Identify the blood parasite species.
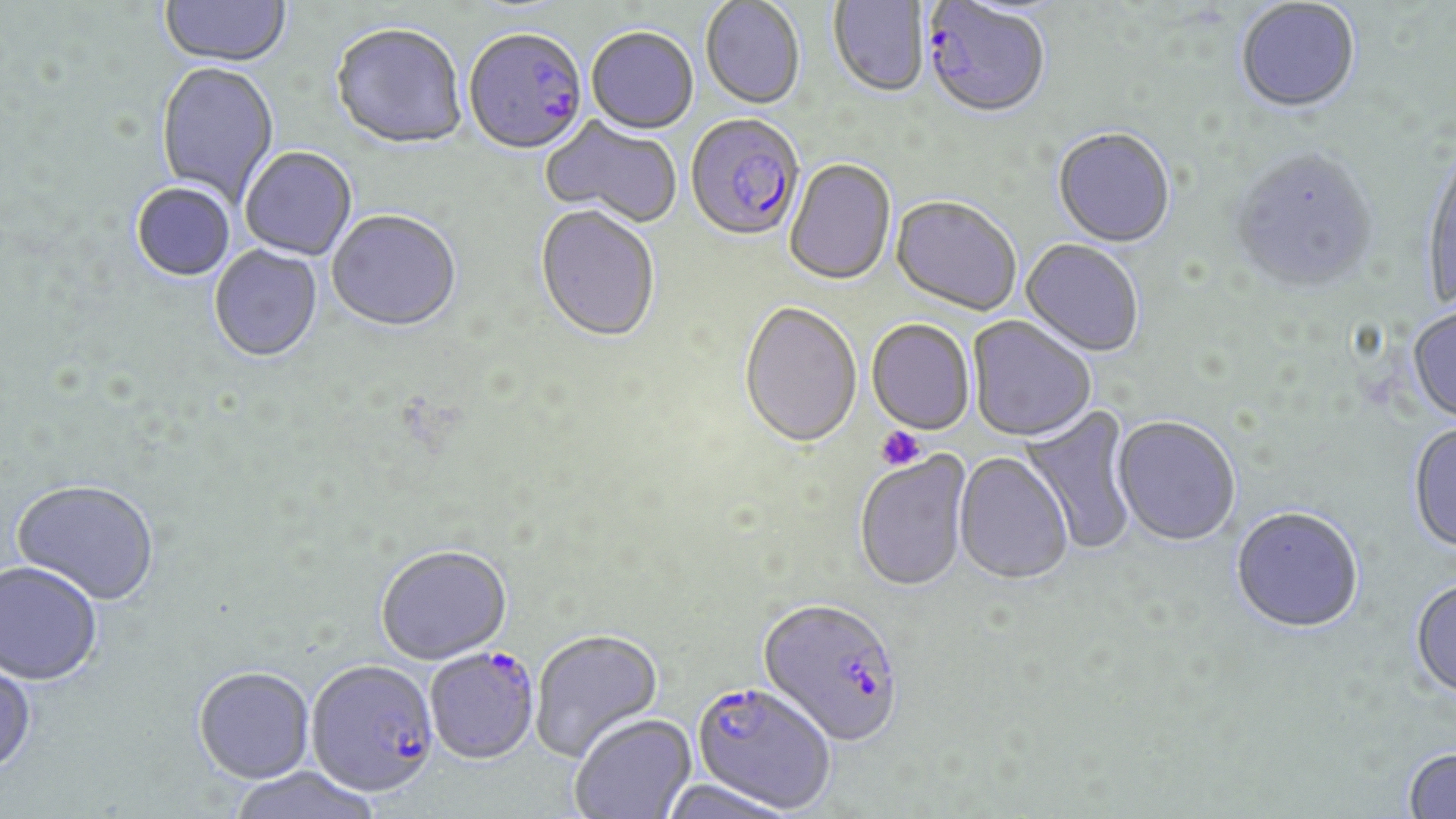

Plasmodium falciparum.

Summary:
  - Coordinate format: approximate bounding boxes as [x1, y1, x2, y2] in pixels
  - Platelet locations: [875, 426, 925, 471]
  - Uninfected red blood cell locations: [160, 1, 291, 69], [700, 1, 805, 112], [829, 1, 930, 100], [1236, 2, 1361, 116], [331, 25, 468, 152], [586, 29, 698, 136], [156, 63, 279, 208], [541, 117, 682, 228], [1053, 130, 1176, 250], [240, 148, 357, 261], [1228, 150, 1379, 297], [1420, 151, 1455, 312], [784, 160, 896, 287], [131, 183, 235, 282], [891, 198, 1021, 317], [534, 207, 660, 345], [327, 212, 462, 335], [1021, 240, 1144, 358], [209, 246, 323, 364], [738, 304, 862, 452], [1407, 308, 1456, 425], [967, 317, 1095, 444], [866, 320, 975, 437], [1018, 402, 1139, 554], [1112, 418, 1241, 547], [1407, 424, 1456, 554], [853, 452, 973, 594], [954, 453, 1073, 587], [12, 479, 160, 606], [1231, 509, 1364, 636], [375, 544, 512, 664], [0, 560, 103, 685], [1410, 580, 1456, 702], [530, 629, 663, 762], [0, 658, 37, 776], [193, 665, 315, 783], [570, 714, 697, 819], [1402, 749, 1456, 818], [227, 767, 383, 819], [659, 778, 800, 819]
  - Plasmodium falciparum-infected red blood cell locations: [923, 2, 1051, 123], [464, 32, 588, 157], [686, 116, 804, 245], [757, 599, 904, 747], [424, 648, 540, 764], [305, 658, 439, 797], [690, 682, 835, 814]
  - Stain: May-Grünwald-Giemsa
  - Magnification: 1000x
  - Modality: optical microscopy
  - Image size: 1456×819 pixels
  - Field of view: one of a larger specimen
  - Preparation: thin blood film